Locate platelets.
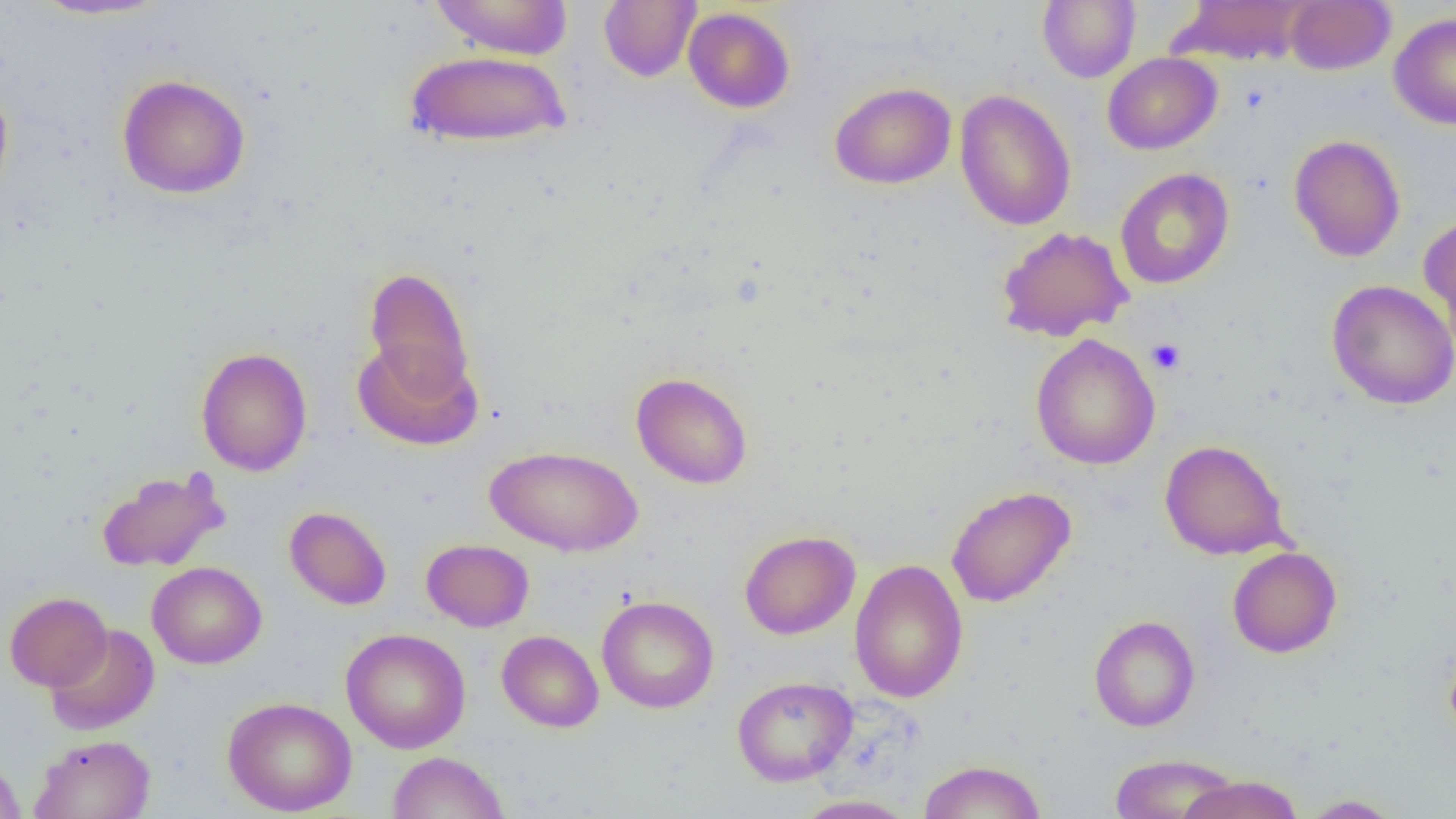

Approximate bounding boxes as named x1/y1/x2/y2 corners in pixels.
Platelets: (x1=1147, y1=338, x2=1185, y2=374).

slide-level diagnosis = negative for blood parasites
uninfected red blood cell locations = approximate bounding boxes as named x1/y1/x2/y2 corners in pixels: (x1=28, y1=0, x2=171, y2=21), (x1=429, y1=0, x2=573, y2=60), (x1=599, y1=0, x2=701, y2=82), (x1=1038, y1=0, x2=1141, y2=83), (x1=1174, y1=0, x2=1313, y2=65), (x1=1285, y1=0, x2=1395, y2=75), (x1=683, y1=7, x2=795, y2=113), (x1=1389, y1=12, x2=1456, y2=130), (x1=404, y1=49, x2=571, y2=148), (x1=1102, y1=52, x2=1221, y2=154), (x1=117, y1=73, x2=251, y2=199), (x1=0, y1=79, x2=14, y2=208), (x1=829, y1=82, x2=957, y2=189), (x1=955, y1=89, x2=1076, y2=231), (x1=1289, y1=134, x2=1406, y2=262), (x1=1115, y1=168, x2=1234, y2=289), (x1=1418, y1=212, x2=1456, y2=341), (x1=996, y1=225, x2=1134, y2=342), (x1=363, y1=267, x2=475, y2=398), (x1=1326, y1=280, x2=1456, y2=410), (x1=1030, y1=334, x2=1160, y2=470), (x1=352, y1=337, x2=482, y2=451), (x1=195, y1=346, x2=313, y2=476), (x1=630, y1=372, x2=752, y2=489), (x1=1159, y1=439, x2=1290, y2=560), (x1=485, y1=445, x2=643, y2=557), (x1=95, y1=469, x2=228, y2=573), (x1=946, y1=486, x2=1076, y2=607), (x1=284, y1=506, x2=392, y2=610), (x1=739, y1=529, x2=860, y2=640), (x1=421, y1=538, x2=534, y2=631), (x1=1227, y1=546, x2=1342, y2=658), (x1=849, y1=558, x2=968, y2=703), (x1=147, y1=561, x2=267, y2=669), (x1=4, y1=591, x2=112, y2=692), (x1=596, y1=595, x2=719, y2=713), (x1=1088, y1=614, x2=1200, y2=731), (x1=44, y1=624, x2=159, y2=736), (x1=341, y1=628, x2=471, y2=753), (x1=496, y1=630, x2=604, y2=733), (x1=1443, y1=641, x2=1456, y2=748), (x1=731, y1=675, x2=858, y2=786), (x1=223, y1=696, x2=357, y2=816), (x1=30, y1=733, x2=156, y2=818), (x1=387, y1=751, x2=509, y2=819), (x1=1110, y1=753, x2=1240, y2=818), (x1=0, y1=756, x2=26, y2=819), (x1=916, y1=760, x2=1047, y2=819), (x1=1177, y1=774, x2=1305, y2=819), (x1=792, y1=794, x2=917, y2=818), (x1=1298, y1=794, x2=1405, y2=818)
magnification = 1000x
modality = optical microscopy
field of view = single
image size = 1456×819 pixels
preparation = thin blood smear